Classify this cell by malaria status.
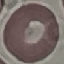

It is uninfected.

Automatically extracted cell patch, resized to 64 × 64 pixels. Photographed with a smartphone camera at the microscope eyepiece. Thin smear of blood. Giemsa-stained preparation.